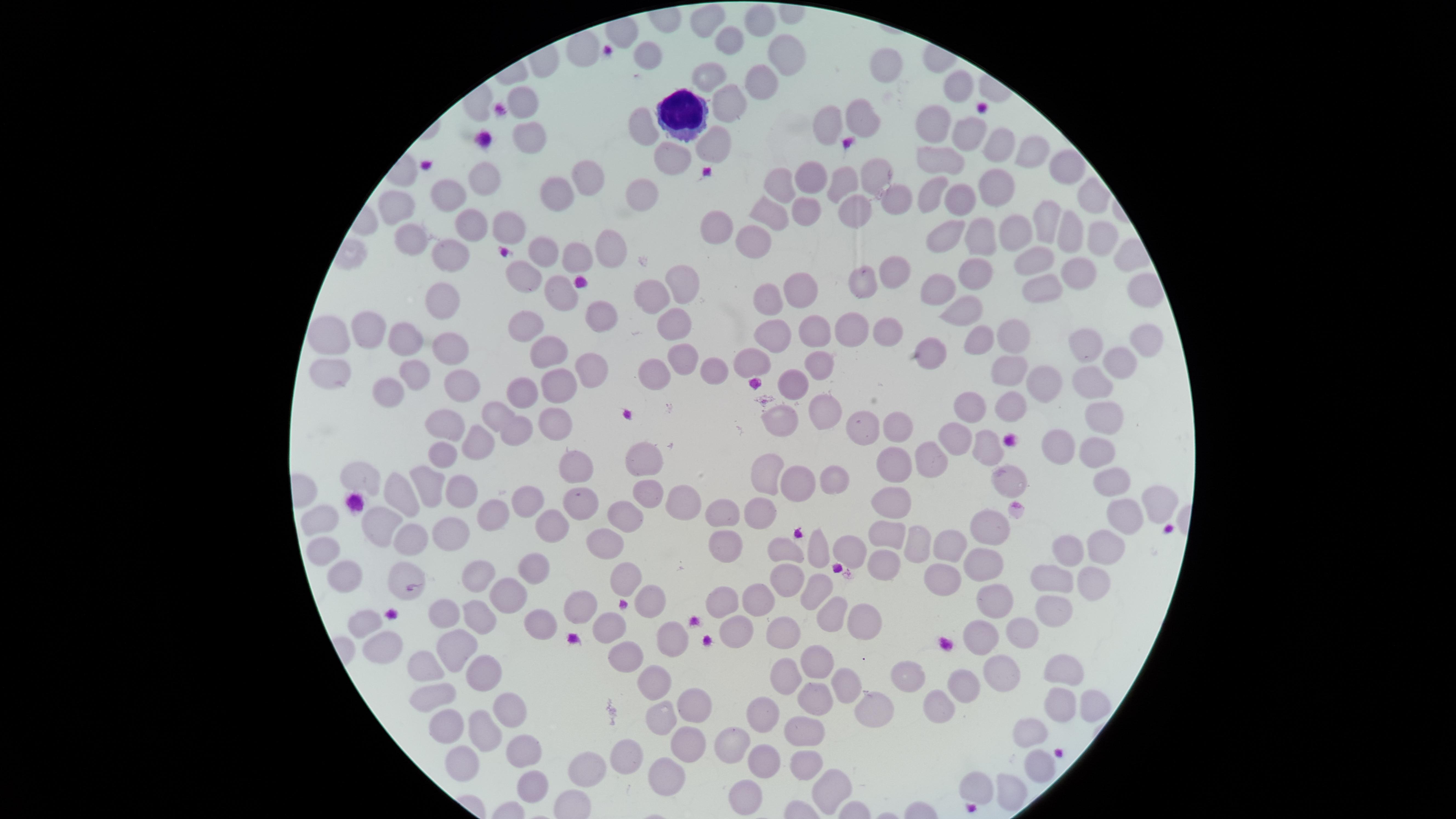 Approximate marker points as {x, y} in pixels. White blood cells: {677, 108}. Uninfected red blood cells: {711, 18}, {768, 26}, {730, 41}, {579, 48}, {786, 60}, {884, 62}, {704, 77}, {957, 84}, {766, 87}, {525, 95}, {726, 106}, {857, 120}, {826, 122}, {934, 122}, {647, 124}, {527, 133}, {971, 133}, {720, 141}, {997, 143}, {1030, 148}, {941, 155}, {674, 156}, {1065, 161}, {875, 172}, {488, 173}, {813, 175}, {585, 178}, {843, 182}, {779, 184}, {995, 188}, {444, 191}, {929, 194}, {551, 195}, {644, 195}, {893, 196}, {960, 199}, {853, 204}, {392, 206}, {769, 208}, {804, 208}, {1050, 211}, {507, 223}, {713, 229}, {1017, 230}, {463, 232}, {950, 232}, {407, 234}, {755, 235}, {984, 236}, {1103, 236}, {1068, 237}, {607, 247}, {544, 248}, {571, 256}, {449, 259}, {1038, 261}, {893, 265}, {1087, 270}, {976, 272}, {524, 273}, {684, 280}, {865, 281}, {1041, 283}, {941, 287}, {800, 288}, {559, 291}, {770, 294}, {654, 295}, {439, 296}, {958, 309}, {605, 310}, {670, 321}, {370, 322}, {524, 323}, {886, 327}, {781, 328}, {1014, 328}, {843, 330}, {331, 333}, {811, 335}, {406, 336}, {1148, 337}, {982, 338}, {1085, 340}, {450, 341}, {552, 349}, {680, 352}, {929, 357}, {1119, 359}, {757, 360}, {821, 361}, {331, 366}, {589, 368}, {656, 370}, {712, 370}, {1014, 370}, {419, 373}, {551, 378}, {463, 383}, {793, 383}, {1090, 383}, {1046, 384}, {524, 393}, {388, 394}, {966, 401}, {1009, 405}, {823, 407}, {499, 410}, {782, 411}, {1103, 414}, {553, 415}, {443, 425}, {868, 427}, {896, 427}, {515, 428}, {957, 430}, {481, 440}, {1058, 441}, {989, 445}, {1095, 449}, {441, 452}, {642, 458}, {932, 459}, {574, 463}, {897, 466}, {766, 468}, {833, 469}, {365, 474}, {1011, 478}, {799, 479}, {1115, 481}, {426, 482}, {649, 489}, {459, 494}, {683, 494}, {896, 495}, {1154, 495}, {393, 496}, {589, 496}, {525, 499}, {627, 511}, {726, 512}, {761, 513}, {494, 515}, {553, 516}, {1117, 517}, {323, 518}, {382, 518}, {996, 523}, {888, 533}, {447, 535}, {411, 536}, {608, 538}, {952, 539}, {725, 542}, {1101, 542}, {326, 544}, {915, 544}, {1072, 545}, {853, 548}, {785, 551}, {820, 552}, {885, 564}, {982, 565}, {346, 569}, {480, 570}, {534, 570}, {408, 572}, {944, 577}, {621, 578}, {1059, 578}, {1091, 580}, {782, 581}, {818, 586}, {509, 593}, {727, 599}, {582, 600}, {755, 600}, {997, 601}, {653, 602}, {1056, 605}, {832, 609}, {449, 610}, {477, 617}, {865, 618}, {735, 619}, {539, 620}, {609, 622}, {366, 623}, {1024, 627}, {778, 631}, {671, 636}, {383, 639}, {976, 640}, {463, 650}, {621, 656}, {817, 662}, {426, 663}, {1009, 669}, {1061, 669}, {483, 670}, {913, 671}, {785, 673}, {655, 678}, {843, 683}, {962, 683}, {434, 690}, {694, 700}, {816, 703}, {933, 705}, {1053, 706}, {1088, 707}, {877, 710}, {504, 713}, {757, 715}, {658, 719}, {445, 726}, {481, 730}, {806, 733}, {1031, 733}, {736, 742}, {687, 747}, {521, 751}, {462, 753}, {622, 753}, {802, 761}, {763, 765}, {1035, 769}, {589, 770}, {665, 774}, {975, 782}, {523, 783}, {827, 785}, {1007, 787}, {744, 792}. Smartphone photograph through the microscope eyepiece. Image is 1456×819 pixels. Giemsa stain. Thin smear of blood. Circular visible region. Presence: no malaria parasites detected. Single field of view.